State which parasite is depicted.
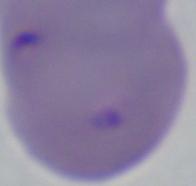
This is Babesia.

Captured at 1000x magnification. Photomicrograph.